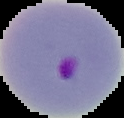
Summary:
  - Preparation: thin blood film
  - Image type: cell region segmented out of the field of view; surrounding area masked to black
  - Malaria status: parasitized
  - Image size: 124×118 pixels